Assess this cell for malaria.
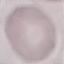
Uninfected.

Photographed with a smartphone camera at the microscope eyepiece. Giemsa stain. Thin blood smear. Cell patch, automatically extracted from a larger field of view and resized to 64 × 64 pixels.